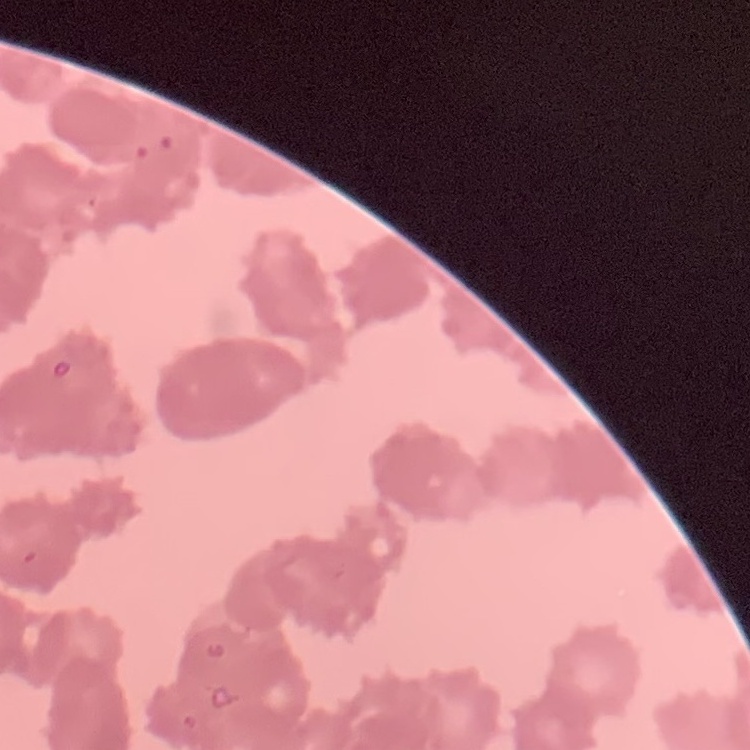

{
  "erythrocyte_morphology": "rouleaux formation",
  "preparation": "thin blood smear",
  "image_type": "square crop of a larger photomicrograph",
  "stain": "Field's or Giemsa"
}